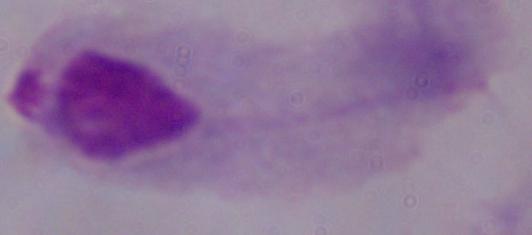
Summary:
  - Modality: micrograph
  - Magnification: 1000x
  - Identification: trichomonad